Comment on the morphology of the red blood cells.
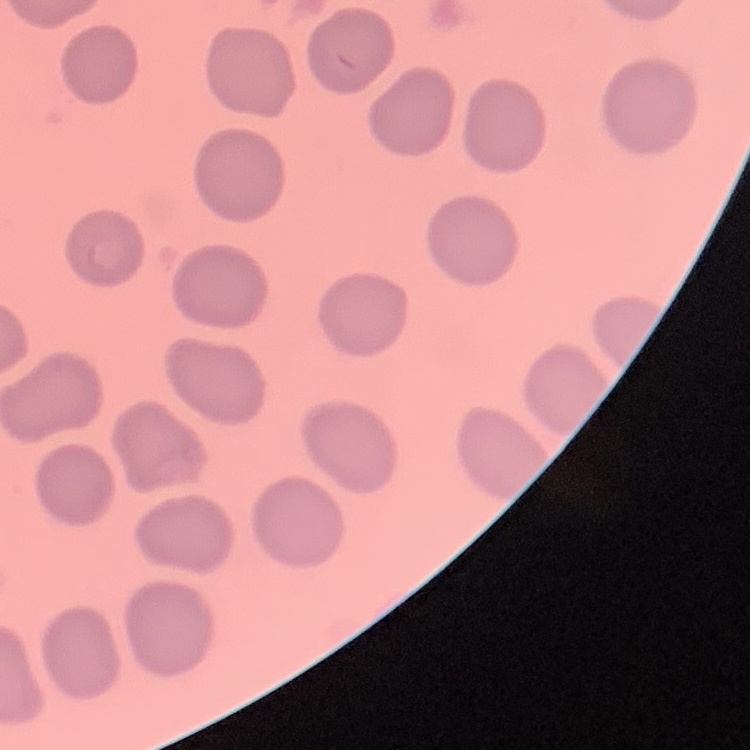
No rouleaux formation.

{
  "image_type": "one tile cut from a larger photomicrograph",
  "preparation": "thin blood smear",
  "stain": "Field's or Giemsa"
}